Give the extent of all uninfected red blood cells.
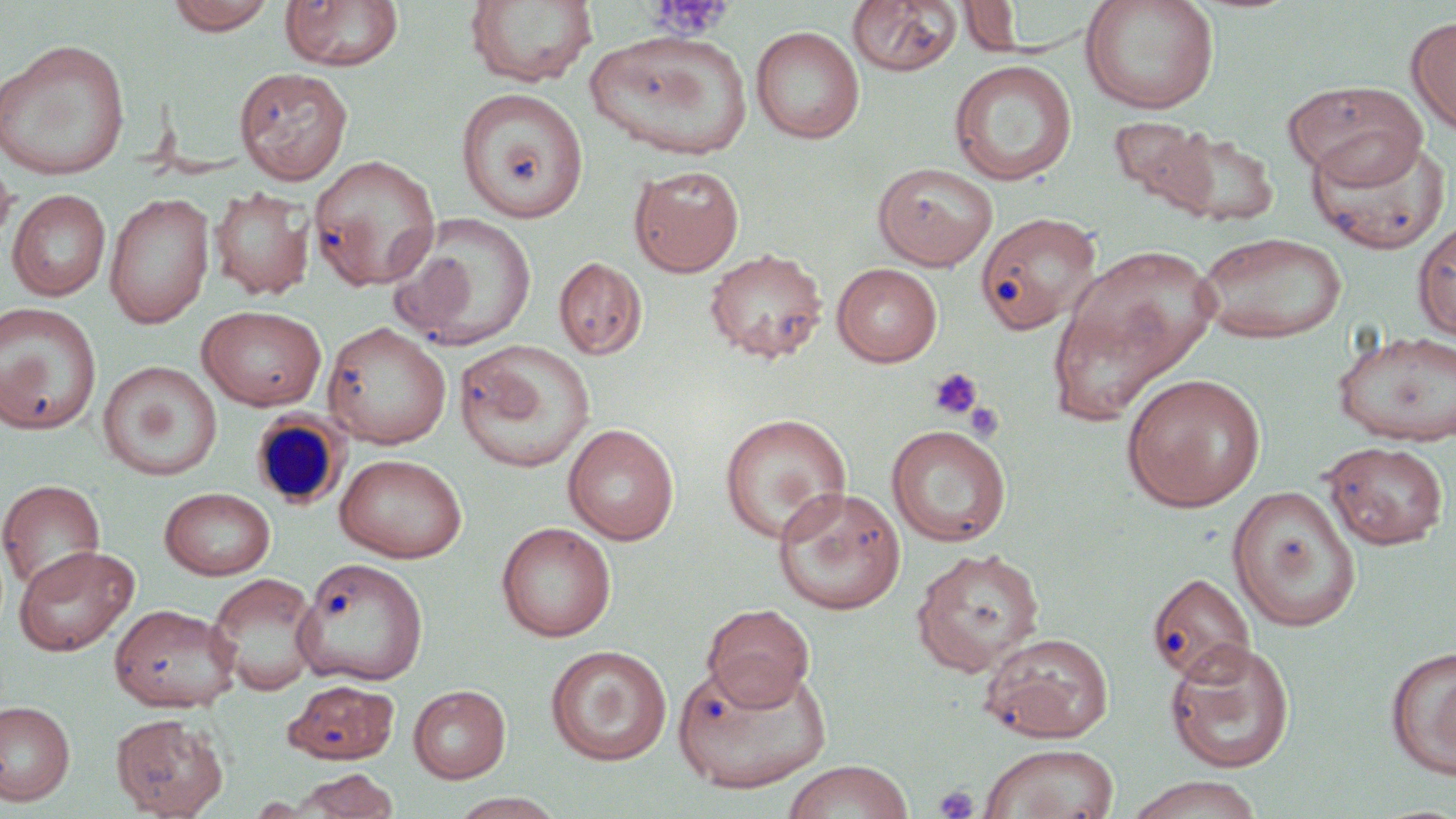

Approximate bounding boxes as named x1/y1/x2/y2 corners in pixels.
Uninfected red blood cells: (x1=165, y1=0, x2=276, y2=34), (x1=279, y1=0, x2=404, y2=71), (x1=464, y1=0, x2=598, y2=88), (x1=958, y1=0, x2=1027, y2=55), (x1=1079, y1=0, x2=1220, y2=115), (x1=846, y1=1, x2=962, y2=77), (x1=1406, y1=15, x2=1456, y2=136), (x1=750, y1=25, x2=865, y2=144), (x1=585, y1=29, x2=753, y2=161), (x1=0, y1=39, x2=132, y2=180), (x1=949, y1=60, x2=1077, y2=186), (x1=234, y1=66, x2=353, y2=184), (x1=1283, y1=81, x2=1429, y2=186), (x1=456, y1=88, x2=589, y2=224), (x1=1110, y1=116, x2=1215, y2=211), (x1=1160, y1=130, x2=1279, y2=227), (x1=1305, y1=132, x2=1452, y2=254), (x1=0, y1=153, x2=16, y2=251), (x1=308, y1=154, x2=441, y2=291), (x1=872, y1=161, x2=999, y2=270), (x1=629, y1=164, x2=744, y2=276), (x1=209, y1=186, x2=314, y2=300), (x1=6, y1=189, x2=110, y2=301), (x1=104, y1=192, x2=215, y2=329), (x1=975, y1=211, x2=1102, y2=334), (x1=388, y1=214, x2=538, y2=351), (x1=1413, y1=219, x2=1456, y2=345), (x1=1194, y1=231, x2=1348, y2=344), (x1=1064, y1=244, x2=1222, y2=383), (x1=704, y1=248, x2=828, y2=364), (x1=553, y1=255, x2=647, y2=360), (x1=831, y1=262, x2=944, y2=366), (x1=1045, y1=297, x2=1182, y2=427), (x1=0, y1=301, x2=102, y2=435), (x1=197, y1=304, x2=327, y2=411), (x1=322, y1=321, x2=452, y2=449), (x1=1333, y1=328, x2=1456, y2=446), (x1=454, y1=340, x2=595, y2=473), (x1=98, y1=361, x2=222, y2=481), (x1=1121, y1=373, x2=1266, y2=512), (x1=719, y1=412, x2=852, y2=544), (x1=563, y1=423, x2=680, y2=545), (x1=885, y1=424, x2=1012, y2=547), (x1=1323, y1=442, x2=1449, y2=550), (x1=334, y1=453, x2=467, y2=563), (x1=0, y1=478, x2=105, y2=594), (x1=1227, y1=485, x2=1362, y2=632), (x1=772, y1=486, x2=906, y2=615), (x1=159, y1=487, x2=276, y2=579), (x1=496, y1=522, x2=616, y2=642), (x1=13, y1=544, x2=140, y2=656), (x1=910, y1=547, x2=1046, y2=677), (x1=293, y1=557, x2=429, y2=686), (x1=206, y1=572, x2=322, y2=695), (x1=1147, y1=572, x2=1256, y2=686), (x1=109, y1=604, x2=240, y2=712), (x1=702, y1=604, x2=815, y2=710), (x1=980, y1=631, x2=1115, y2=743), (x1=1164, y1=638, x2=1296, y2=774), (x1=545, y1=645, x2=672, y2=766), (x1=1384, y1=646, x2=1456, y2=779), (x1=674, y1=660, x2=833, y2=794), (x1=284, y1=679, x2=400, y2=765), (x1=408, y1=684, x2=511, y2=783), (x1=0, y1=700, x2=75, y2=806), (x1=110, y1=713, x2=228, y2=818), (x1=978, y1=743, x2=1120, y2=819), (x1=781, y1=760, x2=915, y2=819), (x1=288, y1=768, x2=401, y2=818), (x1=1124, y1=775, x2=1265, y2=819), (x1=449, y1=792, x2=566, y2=818).

Summary:
  - Platelet locations: (x1=648, y1=1, x2=732, y2=39), (x1=928, y1=366, x2=983, y2=420), (x1=941, y1=385, x2=1004, y2=433), (x1=965, y1=402, x2=1005, y2=442), (x1=933, y1=784, x2=979, y2=819)
  - White blood cell locations: (x1=250, y1=411, x2=351, y2=511)
  - Slide-level diagnosis: no evidence of blood parasites
  - Image size: 1456×819 pixels
  - Stain: May-Grünwald-Giemsa
  - Magnification: 1000x
  - Field of view: one of a larger specimen
  - Preparation: thin blood film
  - Modality: light microscopy